Classify this cell by malaria status.
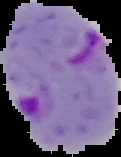
It is parasitized.

Summary:
  - Image type: cell region segmented out of the field of view; surrounding area masked to black
  - Image size: 121×157 pixels
  - Preparation: thin blood smear